Identify the parasite.
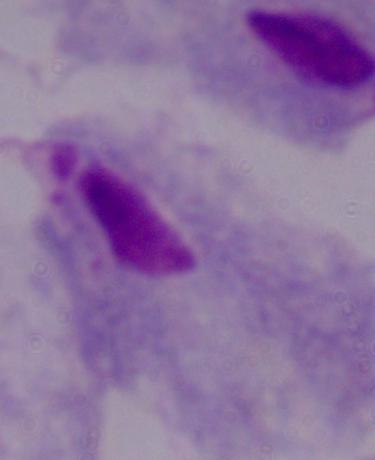

This is a trichomonad.

Summary:
  - Magnification: 1000x
  - Modality: photomicrograph